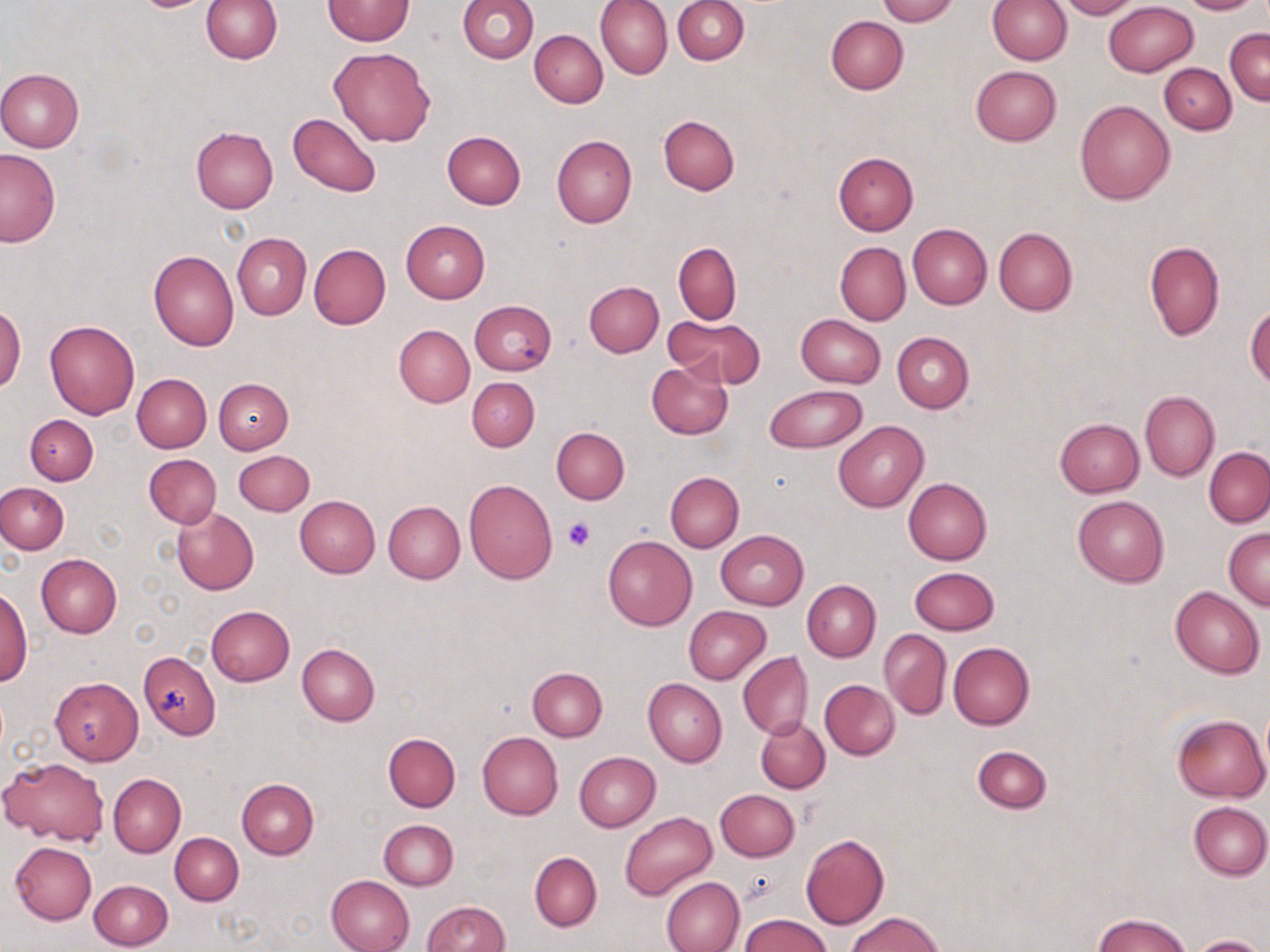
{
  "slide_level_diagnosis": "no evidence of blood parasites",
  "field_of_view": "one of a larger specimen",
  "image_size": "1270×952 pixels",
  "preparation": "thin blood smear",
  "stain": "May-Grünwald-Giemsa",
  "magnification": "1000x",
  "platelet_locations": "approximate bounding boxes as (x1,y1)-(x2,y2) corner pairs in pixels: (563,518)-(595,551)",
  "uninfected_red_blood_cell_locations": "approximate bounding boxes as (x1,y1)-(x2,y2) corner pairs in pixels: (200,0)-(281,64), (323,0)-(414,45), (596,0)-(673,80), (877,0)-(956,24), (988,0)-(1072,64), (1056,0)-(1141,20), (1179,0)-(1259,14), (457,1)-(538,64), (673,1)-(748,63), (1104,1)-(1198,77), (534,12)-(665,88), (826,15)-(909,94), (1225,27)-(1270,104), (529,30)-(608,107), (329,47)-(435,146), (1159,64)-(1236,134), (971,65)-(1061,146), (0,68)-(84,153), (1074,100)-(1175,205), (287,113)-(382,196), (658,116)-(739,195), (190,127)-(278,213), (442,131)-(526,209), (551,135)-(637,228), (0,149)-(61,248), (833,152)-(917,236), (401,219)-(490,302), (908,224)-(991,309), (993,226)-(1077,316), (233,233)-(311,319), (1144,239)-(1225,340), (834,242)-(910,324), (308,243)-(391,329), (673,243)-(741,323), (148,250)-(239,350), (584,281)-(663,356), (469,300)-(555,375), (1245,303)-(1270,388), (0,305)-(26,393), (796,313)-(886,387), (666,314)-(765,387), (44,319)-(140,419), (393,324)-(474,409), (892,332)-(973,413), (645,361)-(733,439), (132,373)-(211,452), (467,377)-(540,451), (213,379)-(293,454), (766,383)-(868,453), (1140,391)-(1219,480), (25,414)-(98,485), (1054,417)-(1143,496), (832,420)-(928,512), (552,427)-(629,503), (1205,446)-(1270,527), (233,450)-(314,516), (144,453)-(221,529), (666,471)-(743,551), (464,478)-(558,584), (903,478)-(992,565), (0,483)-(69,554), (3,488)-(80,606), (294,495)-(380,577), (1072,495)-(1169,587), (383,501)-(465,583), (171,507)-(258,594), (1223,528)-(1270,609), (716,529)-(808,609), (602,535)-(697,630), (37,554)-(122,638), (910,566)-(1000,634), (802,579)-(881,661), (1170,586)-(1264,678), (0,587)-(32,687), (205,606)-(295,686), (684,607)-(771,684), (879,629)-(952,719), (948,641)-(1034,729), (297,644)-(379,726), (138,650)-(220,737), (737,652)-(813,739), (527,667)-(607,741), (50,678)-(143,764), (644,678)-(727,766), (821,680)-(901,759), (1172,714)-(1268,801), (756,717)-(830,793), (384,732)-(461,812), (478,732)-(563,819), (973,746)-(1051,814), (574,752)-(661,831), (1,755)-(110,846), (109,774)-(185,856), (236,778)-(319,859), (715,788)-(799,860), (1188,801)-(1270,879), (620,812)-(717,900), (379,819)-(458,889), (170,832)-(243,905), (801,834)-(890,930), (9,842)-(97,925), (529,852)-(601,932), (326,875)-(414,952), (661,876)-(744,952), (89,879)-(173,950), (423,901)-(508,951), (845,912)-(946,952), (741,914)-(832,952), (1093,914)-(1191,952), (1191,935)-(1265,952)",
  "modality": "light microscopy"
}